Assess this cell for malaria.
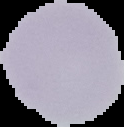
It is uninfected.

Summary:
  - Preparation: thin blood smear
  - Image type: segmented cell region with the area outside set to black
  - Image size: 124×127 pixels